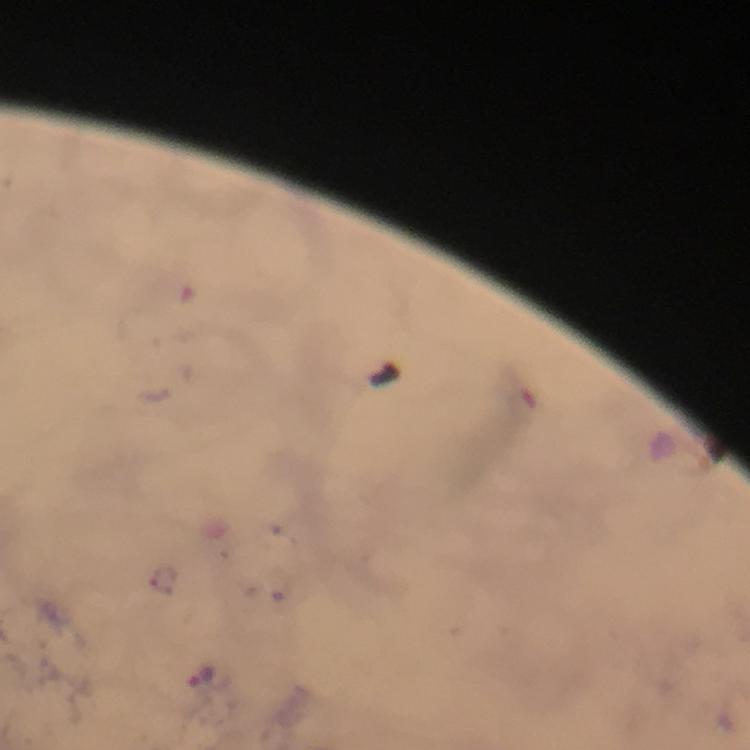 Approximate object centers, in pixels from the top-left corner. Malaria parasite locations: (x=202, y=674). From a malaria diagnostic workup. Image is 750×750 pixels. Cropped region of a single field of view. 100x magnification. Giemsa stain. Thick smear. Immersion oil was used. Smartphone photograph taken through a microscope.